State which cell type is depicted.
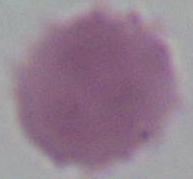
An erythrocyte.

{
  "modality": "micrograph",
  "magnification": "1000x"
}